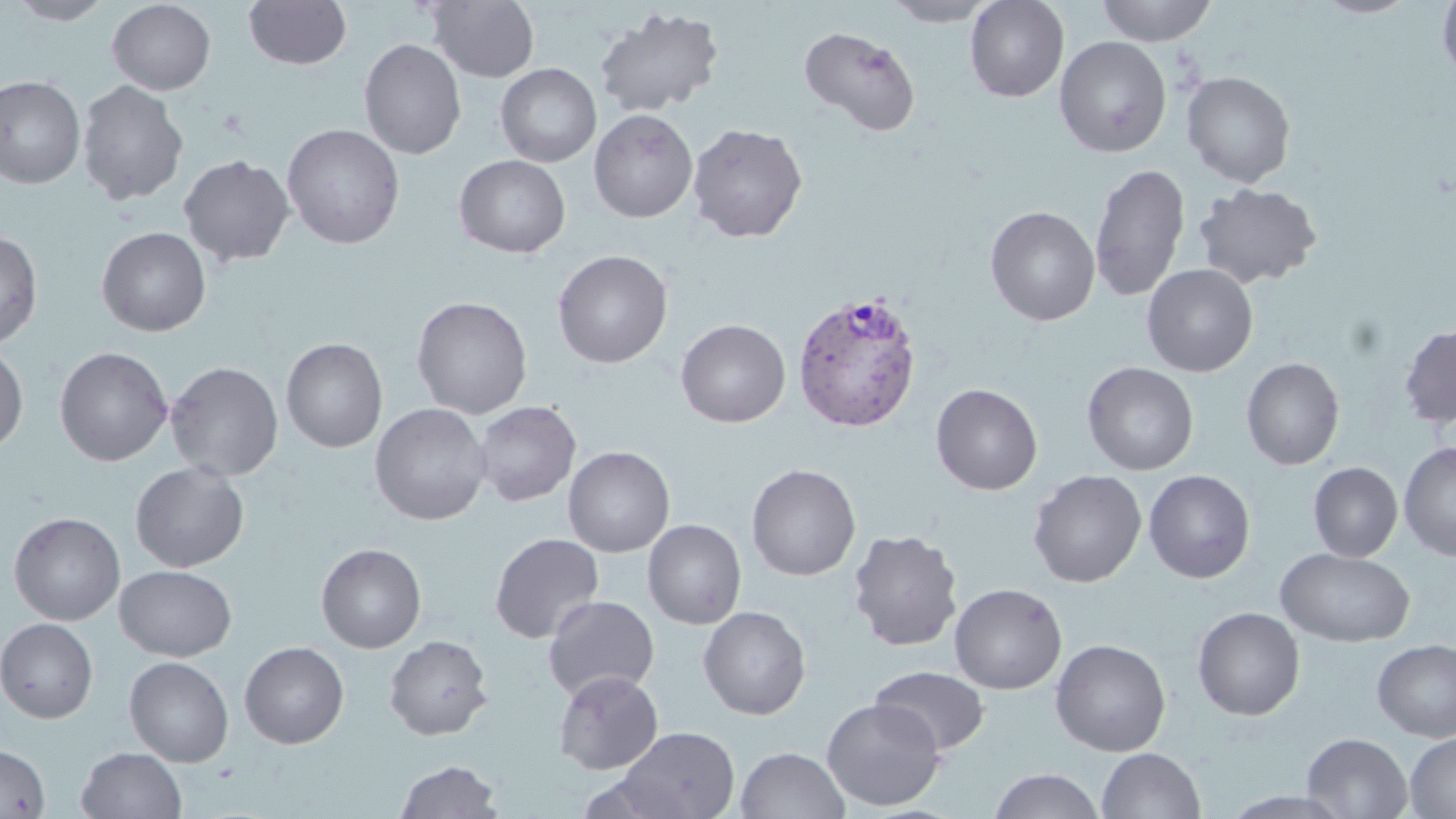
Summary:
  - Coordinate format: approximate bounding boxes as (x1, y1, x2, y2) in pixels
  - Plasmodium vivax-infected red blood cell locations: (791, 289, 923, 433)
  - Uninfected red blood cell locations: (4, 0, 115, 25), (243, 0, 353, 70), (427, 0, 540, 82), (883, 0, 999, 27), (965, 0, 1069, 102), (1095, 0, 1217, 46), (1313, 0, 1420, 18), (1437, 0, 1456, 85), (106, 1, 216, 95), (594, 6, 725, 117), (799, 25, 921, 137), (1054, 36, 1172, 157), (359, 38, 466, 159), (495, 63, 602, 167), (1182, 70, 1296, 187), (0, 75, 86, 189), (76, 80, 188, 205), (588, 108, 698, 223), (687, 122, 808, 243), (282, 123, 405, 249), (179, 154, 295, 267), (454, 154, 571, 258), (1089, 162, 1190, 301), (1193, 182, 1322, 289), (985, 205, 1100, 326), (97, 226, 211, 336), (0, 230, 43, 350), (553, 250, 672, 369), (1142, 264, 1257, 376), (411, 296, 533, 418), (676, 318, 790, 427), (1399, 323, 1456, 429), (281, 337, 387, 452), (0, 344, 29, 454), (54, 346, 173, 466), (1241, 357, 1344, 470), (166, 361, 283, 482), (1082, 362, 1199, 475), (931, 383, 1043, 495), (473, 400, 580, 506), (370, 403, 490, 525), (1399, 441, 1456, 560), (563, 445, 675, 556), (130, 461, 249, 572), (1308, 462, 1403, 562), (746, 463, 861, 581), (1028, 469, 1147, 587), (1144, 470, 1255, 583), (8, 512, 125, 625), (643, 519, 746, 629), (848, 528, 963, 651), (489, 532, 605, 644), (316, 543, 426, 653), (1275, 547, 1415, 647), (115, 565, 236, 661), (949, 582, 1067, 694), (543, 595, 659, 702), (698, 606, 811, 720), (1192, 606, 1305, 721), (0, 617, 99, 722), (384, 634, 493, 740), (1050, 638, 1171, 756), (1372, 638, 1456, 743), (240, 641, 349, 748), (124, 656, 234, 767), (869, 666, 990, 755), (553, 670, 663, 775), (821, 697, 945, 811), (614, 726, 740, 819), (1404, 732, 1456, 818), (1301, 733, 1413, 818), (0, 744, 50, 819), (76, 747, 186, 819), (735, 747, 849, 819), (1096, 748, 1205, 819), (394, 759, 503, 818), (989, 768, 1104, 819)
  - Slide-level diagnosis: Plasmodium vivax
  - Field of view: single
  - Magnification: 1000x
  - Image size: 1456×819 pixels
  - Preparation: thin blood film
  - Modality: optical microscopy
  - Stain: May-Grünwald-Giemsa